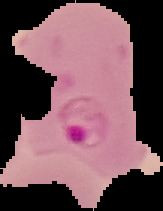
image type = segmented cell region on a black background
malaria status = parasitized
preparation = thin blood film
image size = 163×211 pixels